Describe the morphology of the erythrocytes.
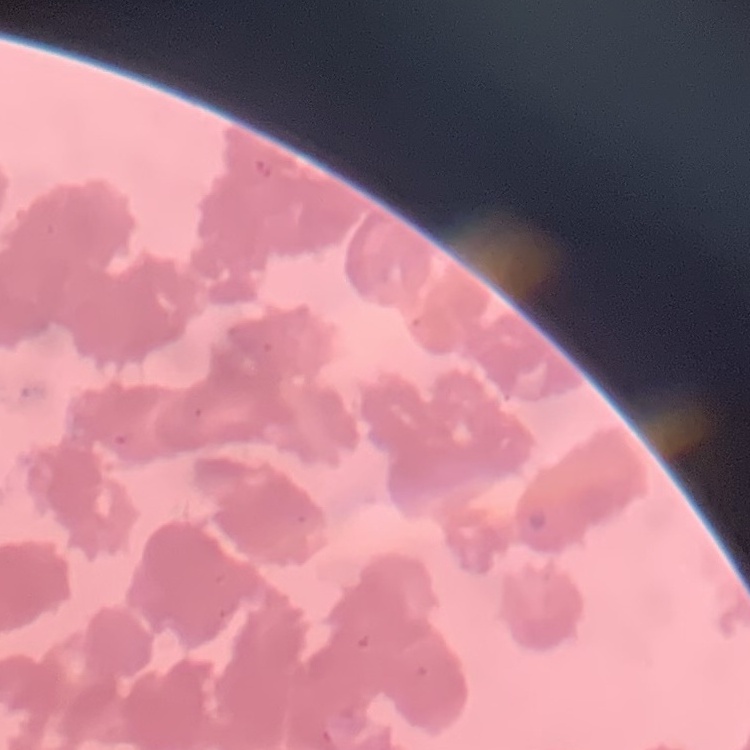
Rouleaux formation.

Thin blood smear. Square crop of a larger photomicrograph. Field's or Giemsa stain.